Assess this cell for malaria.
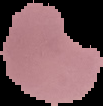
It is parasitized.

preparation: thin blood smear
image_type: segmented cell region with the area outside set to black
image_size: 103×106 pixels